Locate every Plasmodium falciparum-infected red blood cell.
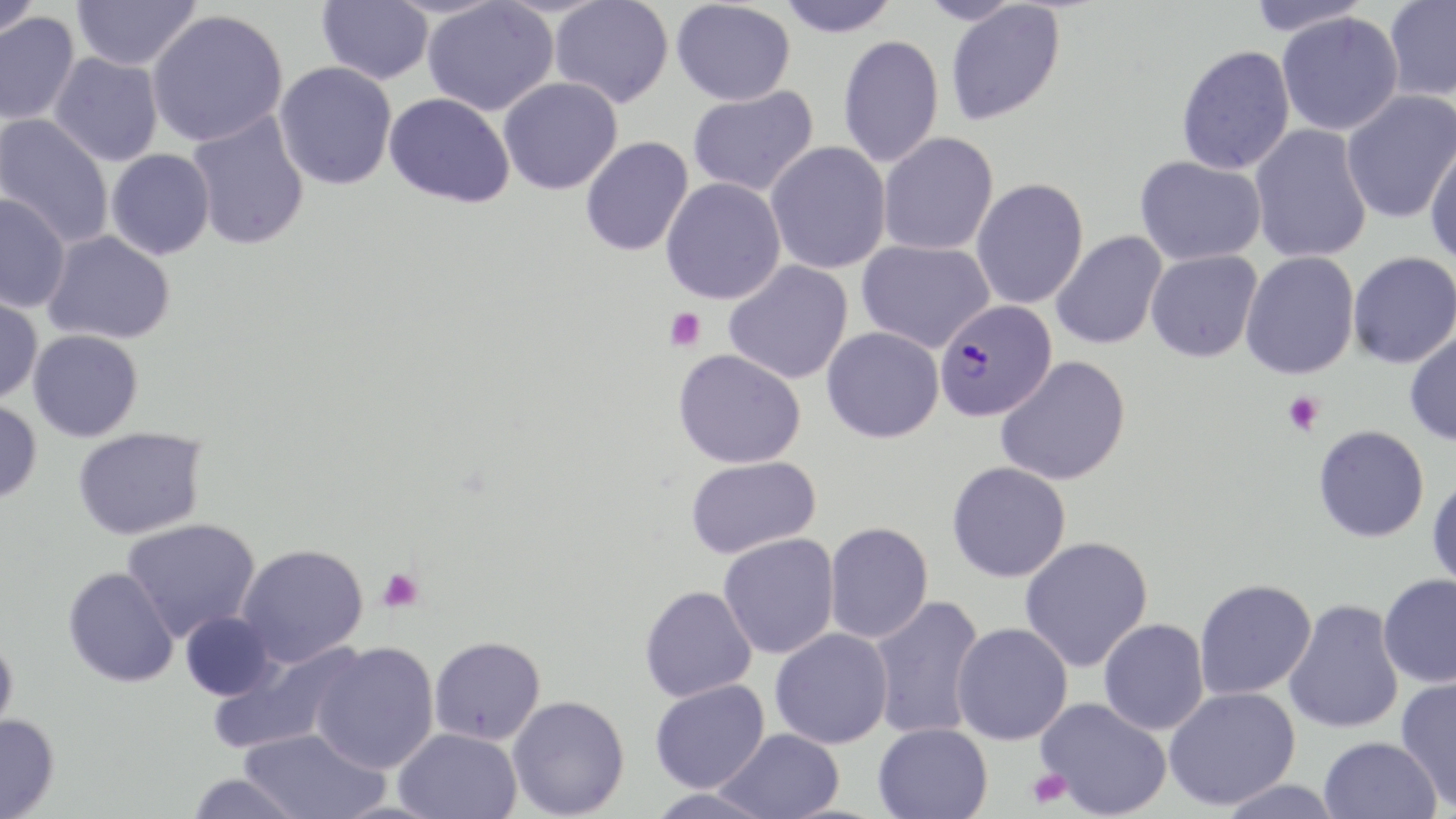

Approximate bounding boxes as named x1/y1/x2/y2 corners in pixels.
Plasmodium falciparum-infected red blood cells: (x1=935, y1=299, x2=1056, y2=421).

{
  "slide_level_diagnosis": "Plasmodium falciparum",
  "stain": "May-Grünwald-Giemsa",
  "platelet_locations": "approximate bounding boxes as named x1/y1/x2/y2 corners in pixels: (x1=665, y1=307, x2=706, y2=352), (x1=1282, y1=390, x2=1325, y2=436), (x1=377, y1=568, x2=424, y2=613), (x1=1027, y1=767, x2=1072, y2=810)",
  "preparation": "thin blood smear",
  "image_size": "1456×819 pixels",
  "magnification": "1000x",
  "field_of_view": "single",
  "modality": "optical microscopy",
  "uninfected_red_blood_cell_locations": "approximate bounding boxes as named x1/y1/x2/y2 corners in pixels: (x1=0, y1=0, x2=41, y2=40), (x1=72, y1=0, x2=200, y2=71), (x1=317, y1=0, x2=434, y2=85), (x1=550, y1=0, x2=673, y2=108), (x1=776, y1=0, x2=900, y2=38), (x1=919, y1=0, x2=1021, y2=26), (x1=1244, y1=0, x2=1371, y2=36), (x1=1383, y1=0, x2=1456, y2=101), (x1=422, y1=1, x2=559, y2=116), (x1=672, y1=1, x2=795, y2=106), (x1=945, y1=2, x2=1066, y2=126), (x1=147, y1=10, x2=288, y2=147), (x1=0, y1=12, x2=80, y2=125), (x1=1277, y1=12, x2=1404, y2=136), (x1=837, y1=34, x2=944, y2=168), (x1=1176, y1=45, x2=1295, y2=175), (x1=49, y1=52, x2=164, y2=166), (x1=274, y1=61, x2=397, y2=190), (x1=498, y1=77, x2=622, y2=195), (x1=687, y1=87, x2=819, y2=197), (x1=1340, y1=89, x2=1456, y2=224), (x1=384, y1=92, x2=515, y2=208), (x1=187, y1=112, x2=310, y2=250), (x1=0, y1=113, x2=115, y2=250), (x1=1250, y1=124, x2=1373, y2=264), (x1=878, y1=132, x2=999, y2=256), (x1=580, y1=136, x2=694, y2=256), (x1=1425, y1=139, x2=1456, y2=267), (x1=765, y1=141, x2=891, y2=274), (x1=105, y1=149, x2=215, y2=259), (x1=1135, y1=155, x2=1266, y2=265), (x1=660, y1=177, x2=787, y2=305), (x1=971, y1=178, x2=1089, y2=309), (x1=0, y1=194, x2=71, y2=313), (x1=1051, y1=230, x2=1167, y2=350), (x1=43, y1=231, x2=175, y2=345), (x1=856, y1=239, x2=994, y2=353), (x1=1145, y1=250, x2=1262, y2=362), (x1=1347, y1=251, x2=1456, y2=369), (x1=1240, y1=252, x2=1360, y2=379), (x1=724, y1=261, x2=853, y2=384), (x1=0, y1=289, x2=43, y2=406), (x1=822, y1=326, x2=944, y2=443), (x1=28, y1=329, x2=143, y2=442), (x1=1404, y1=330, x2=1456, y2=447), (x1=673, y1=349, x2=806, y2=469), (x1=995, y1=356, x2=1131, y2=486), (x1=0, y1=399, x2=42, y2=504), (x1=1313, y1=425, x2=1429, y2=542), (x1=72, y1=427, x2=207, y2=540), (x1=685, y1=456, x2=821, y2=558), (x1=947, y1=461, x2=1072, y2=583), (x1=1427, y1=475, x2=1456, y2=592), (x1=122, y1=519, x2=260, y2=642), (x1=823, y1=522, x2=933, y2=644), (x1=718, y1=534, x2=840, y2=659), (x1=1019, y1=535, x2=1154, y2=672), (x1=237, y1=544, x2=367, y2=667), (x1=63, y1=567, x2=179, y2=688), (x1=1377, y1=573, x2=1456, y2=688), (x1=1194, y1=578, x2=1317, y2=700), (x1=639, y1=585, x2=757, y2=702), (x1=868, y1=595, x2=986, y2=740), (x1=1283, y1=599, x2=1404, y2=734), (x1=179, y1=611, x2=277, y2=701), (x1=1098, y1=619, x2=1209, y2=735), (x1=952, y1=622, x2=1073, y2=745), (x1=769, y1=628, x2=893, y2=749), (x1=0, y1=636, x2=18, y2=742), (x1=429, y1=636, x2=545, y2=745), (x1=311, y1=642, x2=439, y2=774), (x1=206, y1=643, x2=362, y2=756), (x1=1395, y1=675, x2=1456, y2=810), (x1=650, y1=679, x2=769, y2=793), (x1=1163, y1=686, x2=1301, y2=810), (x1=507, y1=695, x2=629, y2=818), (x1=1036, y1=697, x2=1172, y2=818), (x1=0, y1=715, x2=59, y2=819), (x1=873, y1=722, x2=993, y2=819), (x1=393, y1=727, x2=522, y2=819), (x1=239, y1=728, x2=388, y2=819), (x1=716, y1=728, x2=845, y2=819), (x1=1318, y1=736, x2=1442, y2=819), (x1=185, y1=773, x2=305, y2=819), (x1=1212, y1=779, x2=1348, y2=819), (x1=647, y1=787, x2=775, y2=819)"
}